Comment on the morphology of the red blood cells.
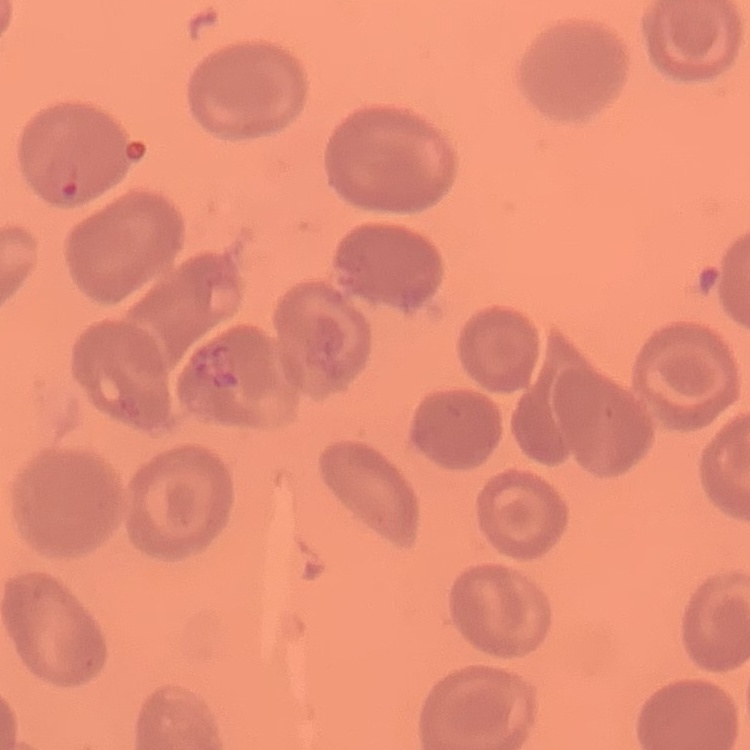
No rouleaux formation.

Summary:
  - Image type: one tile cut from a larger photomicrograph
  - Preparation: thin blood smear
  - Stain: Field's or Giemsa